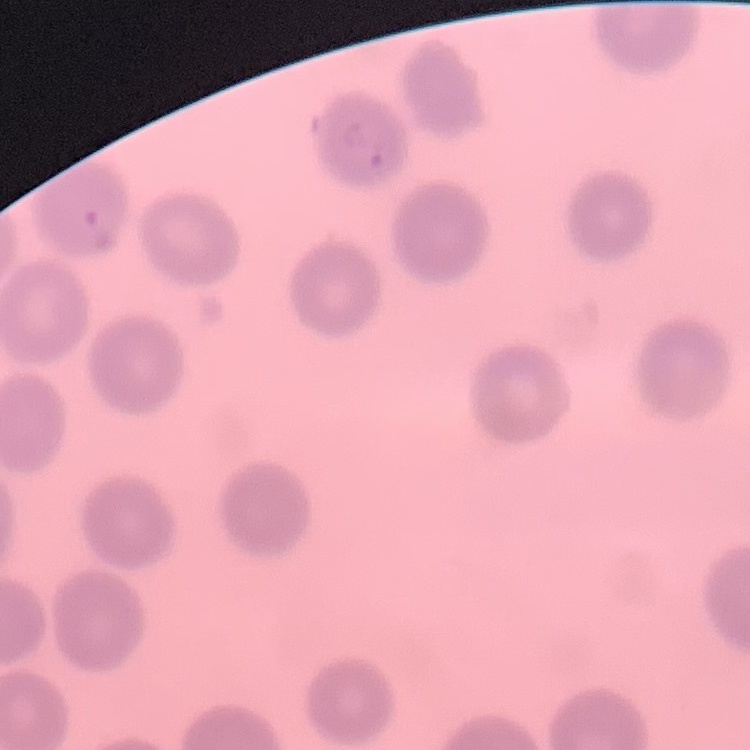

Summary:
  - Red blood cell morphology: no rouleaux formation
  - Image type: one tile cut from a larger photomicrograph
  - Preparation: thin peripheral smear
  - Stain: Field's or Giemsa